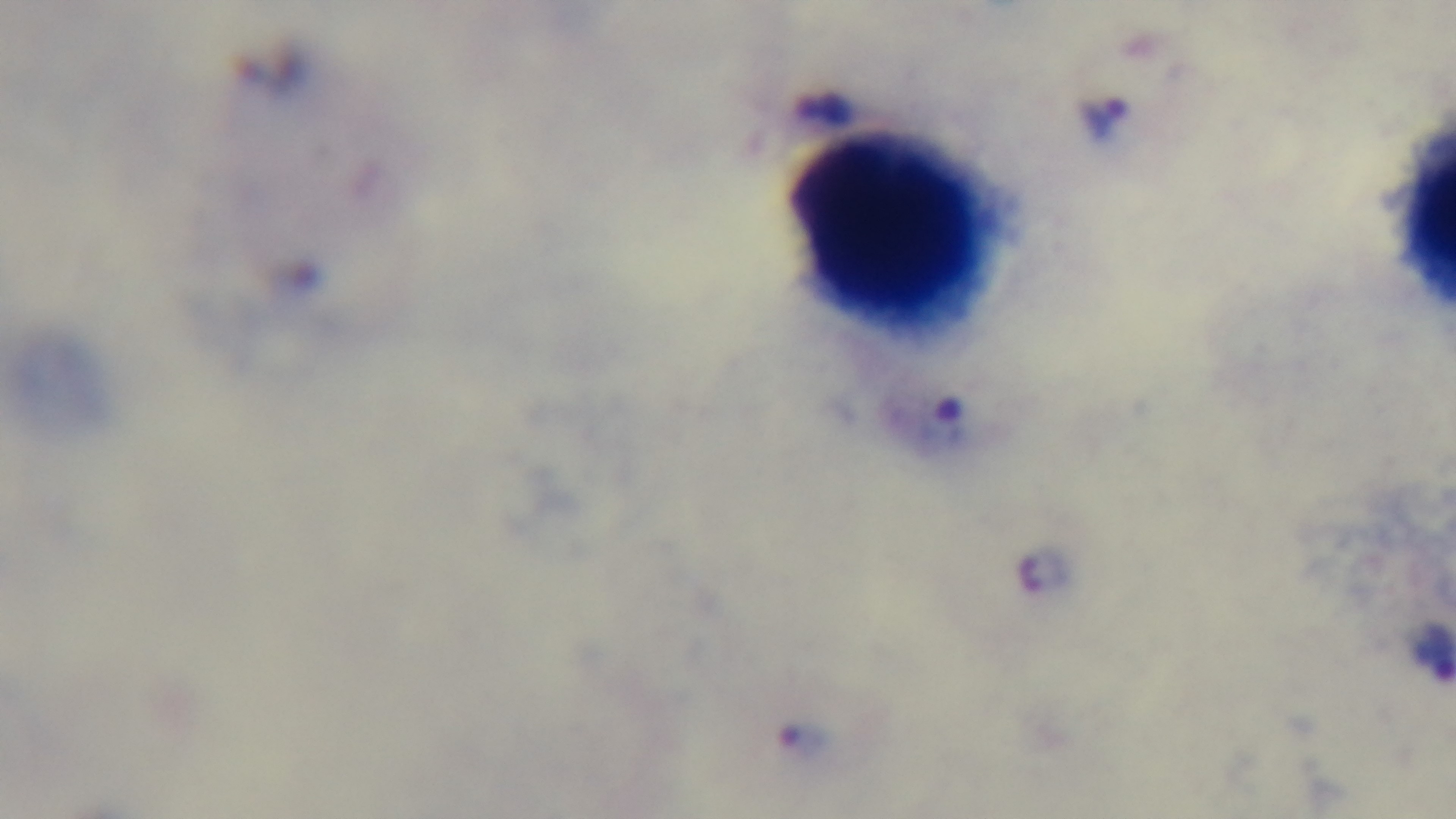
objective = 100x oil immersion
capture = mounted 4K digital camera
modality = light microscopy
field of view = one from the slide
preparation = thick smear
stain = Giemsa
malaria status = positive